Name the parasite shown.
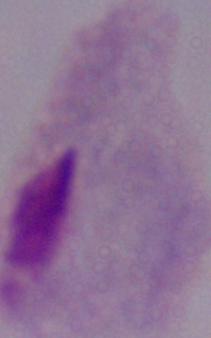
This is a trichomonad.

Micrograph. 1000x magnification.